Locate every blood parasite and identify its species.
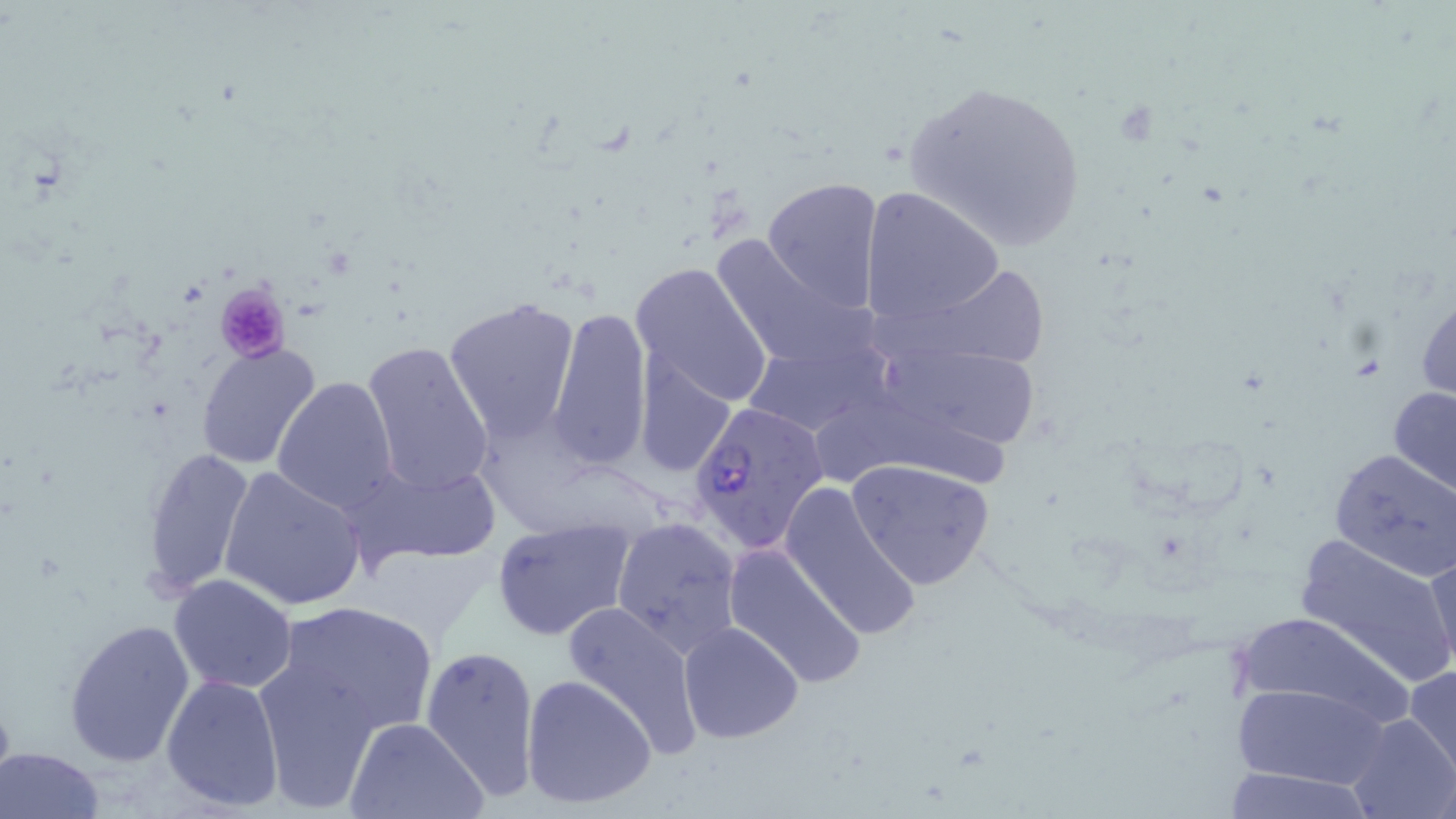

Approximate bounding boxes as named x1/y1/x2/y2 corners in pixels.
Plasmodium falciparum-infected red blood cells: (x1=687, y1=398, x2=829, y2=553).
No Plasmodium ovale, Plasmodium malariae, Plasmodium vivax, Babesia divergens, or Trypanosoma brucei observed.

Summary:
  - Platelet locations: (x1=213, y1=284, x2=293, y2=364)
  - Uninfected red blood cell locations: (x1=898, y1=77, x2=1090, y2=254), (x1=761, y1=177, x2=884, y2=313), (x1=860, y1=185, x2=1004, y2=329), (x1=714, y1=236, x2=880, y2=368), (x1=629, y1=262, x2=775, y2=412), (x1=866, y1=267, x2=1060, y2=373), (x1=442, y1=297, x2=581, y2=446), (x1=546, y1=306, x2=652, y2=471), (x1=361, y1=340, x2=496, y2=497), (x1=194, y1=341, x2=321, y2=468), (x1=868, y1=345, x2=1043, y2=453), (x1=634, y1=353, x2=739, y2=482), (x1=272, y1=375, x2=403, y2=514), (x1=1388, y1=383, x2=1456, y2=500), (x1=810, y1=404, x2=1021, y2=502), (x1=140, y1=446, x2=257, y2=601), (x1=1326, y1=448, x2=1456, y2=580), (x1=342, y1=459, x2=504, y2=568), (x1=846, y1=459, x2=997, y2=591), (x1=218, y1=465, x2=366, y2=612), (x1=779, y1=480, x2=920, y2=640), (x1=491, y1=516, x2=637, y2=641), (x1=612, y1=517, x2=744, y2=658), (x1=1292, y1=532, x2=1456, y2=690), (x1=721, y1=542, x2=869, y2=690), (x1=1423, y1=547, x2=1456, y2=682), (x1=168, y1=573, x2=298, y2=694), (x1=558, y1=597, x2=704, y2=757), (x1=272, y1=600, x2=439, y2=738), (x1=1231, y1=608, x2=1409, y2=731), (x1=64, y1=617, x2=198, y2=767), (x1=678, y1=622, x2=803, y2=743), (x1=421, y1=642, x2=543, y2=801), (x1=253, y1=653, x2=388, y2=812), (x1=1404, y1=663, x2=1456, y2=783), (x1=160, y1=673, x2=287, y2=814), (x1=520, y1=673, x2=657, y2=812), (x1=1230, y1=679, x2=1395, y2=790), (x1=1344, y1=710, x2=1454, y2=819), (x1=345, y1=716, x2=489, y2=819), (x1=0, y1=746, x2=106, y2=819), (x1=1222, y1=763, x2=1375, y2=817)
  - Slide-level diagnosis: Plasmodium falciparum
  - Preparation: thin blood smear
  - Field of view: single
  - Magnification: 1000x
  - Modality: optical microscopy
  - Image size: 1456×819 pixels
  - Stain: May-Grünwald-Giemsa